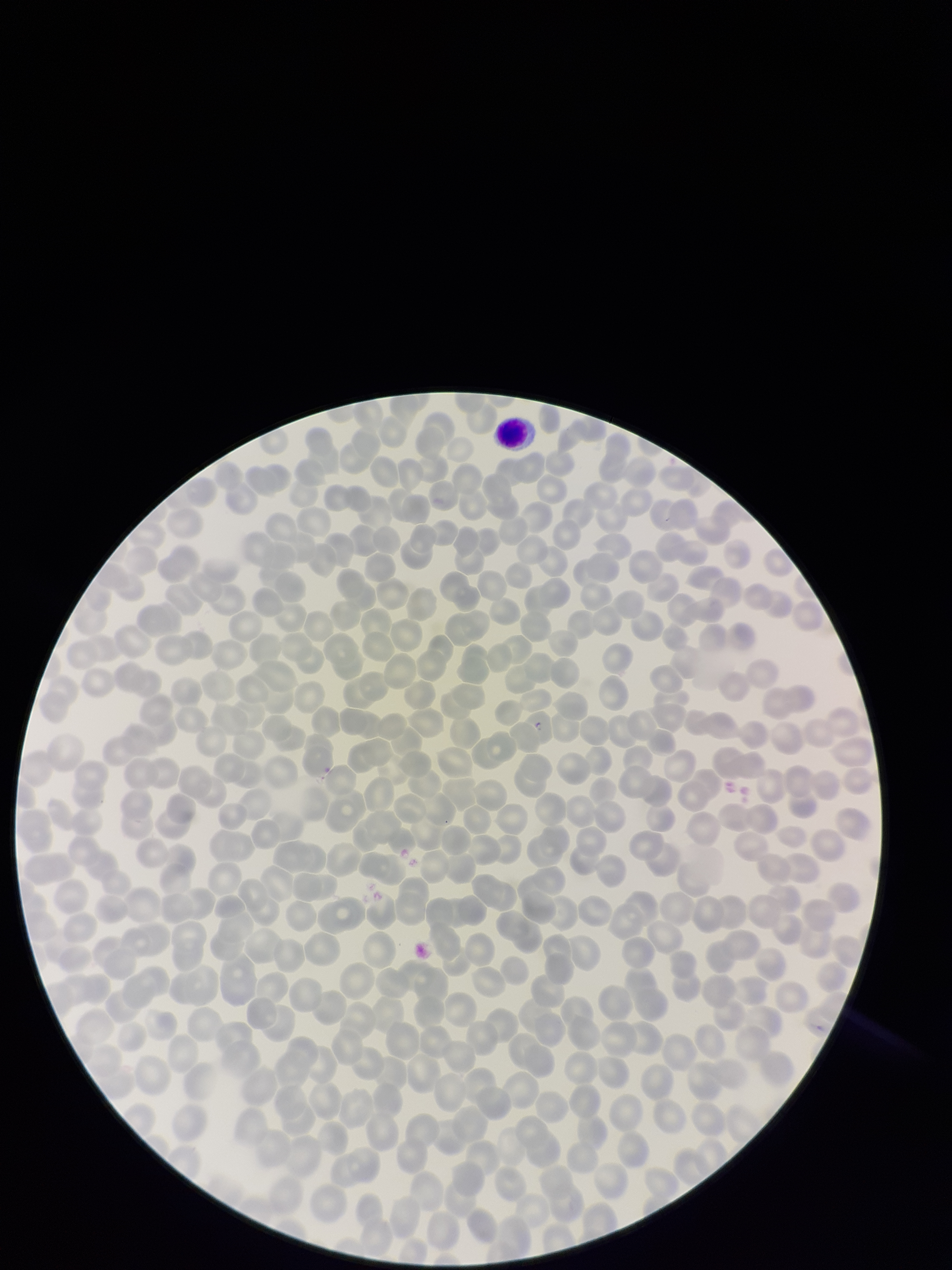

Image is 952×1270 pixels. Species reported for this patient: Plasmodium falciparum. Photographed through the microscope eyepiece with a smartphone camera. Giemsa stain. Parasitized red blood cell count: 0. Patient malaria status: positive. Single field of view. Parasitized red blood cells: none identified. Preparation: thin smear. Red blood cell count: 372.